Locate every uninfected red blood cell.
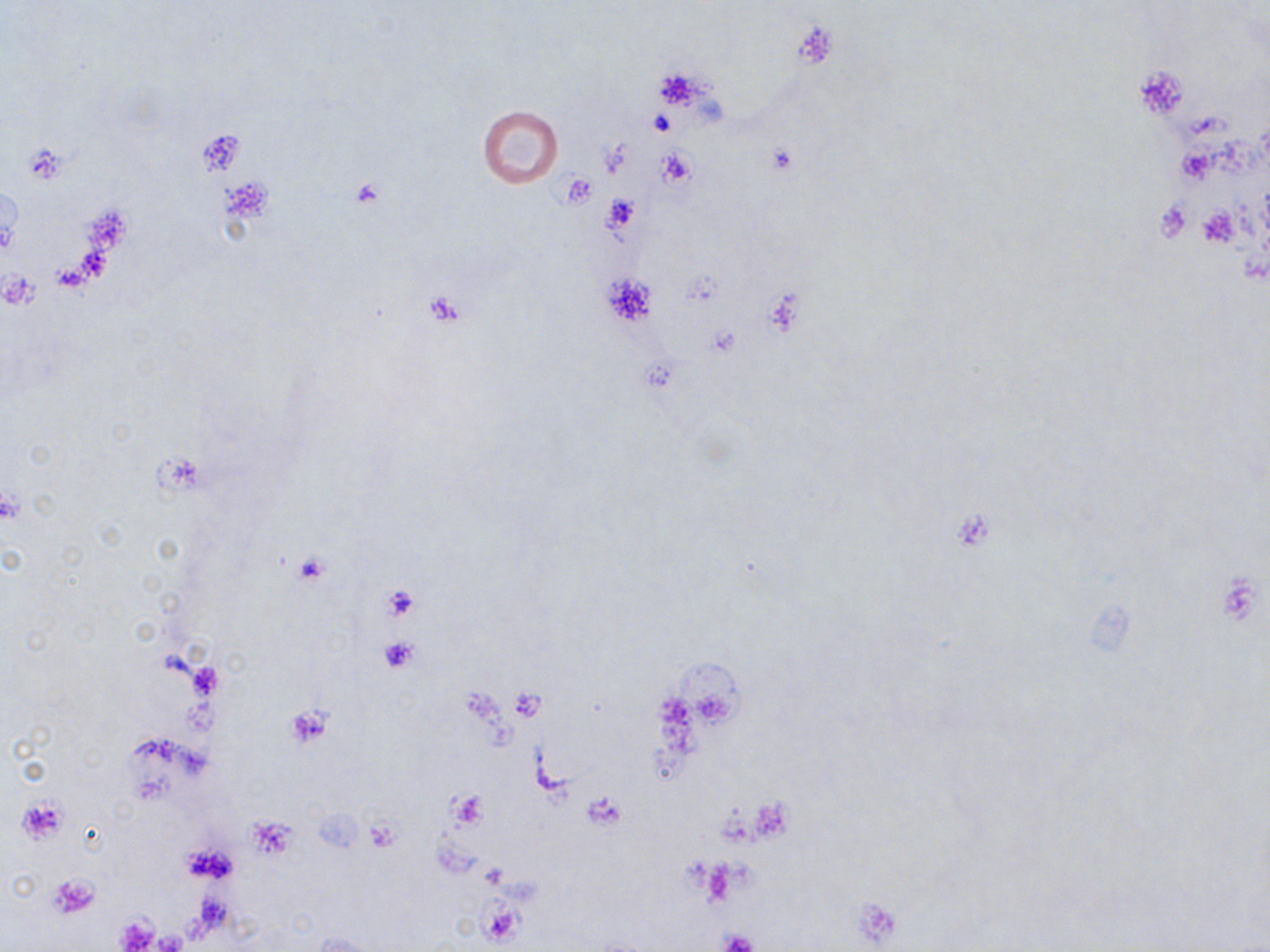

Approximate bounding boxes as (x1,y1)-(x2,y2) corner pairs in pixels.
Uninfected red blood cells: (477,107)-(563,188), (313,932)-(374,951).

{
  "slide_level_diagnosis": "negative for blood parasites",
  "magnification": "1000x",
  "image_size": "1270×952 pixels",
  "stain": "May-Grünwald-Giemsa",
  "field_of_view": "one of a larger specimen",
  "modality": "light microscopy",
  "preparation": "thin blood smear",
  "platelet_locations": "approximate bounding boxes as (x1,y1)-(x2,y2) corner pairs in pixels: (792,21)-(837,69), (1135,65)-(1192,119), (649,109)-(675,136), (767,144)-(796,176), (657,147)-(698,190), (559,173)-(597,208), (350,178)-(386,211), (602,193)-(642,234), (1197,206)-(1240,249), (599,271)-(657,326), (424,290)-(467,325), (0,485)-(24,527), (293,554)-(330,586), (383,585)-(419,621), (377,637)-(420,672), (284,706)-(333,748), (447,789)-(486,831), (584,793)-(626,830), (16,796)-(68,844), (249,818)-(296,856), (366,819)-(402,851), (184,842)-(237,884), (49,874)-(100,918), (853,896)-(903,947), (478,899)-(526,947), (114,914)-(160,952), (719,929)-(760,952)"
}